Locate and identify every blood parasite.
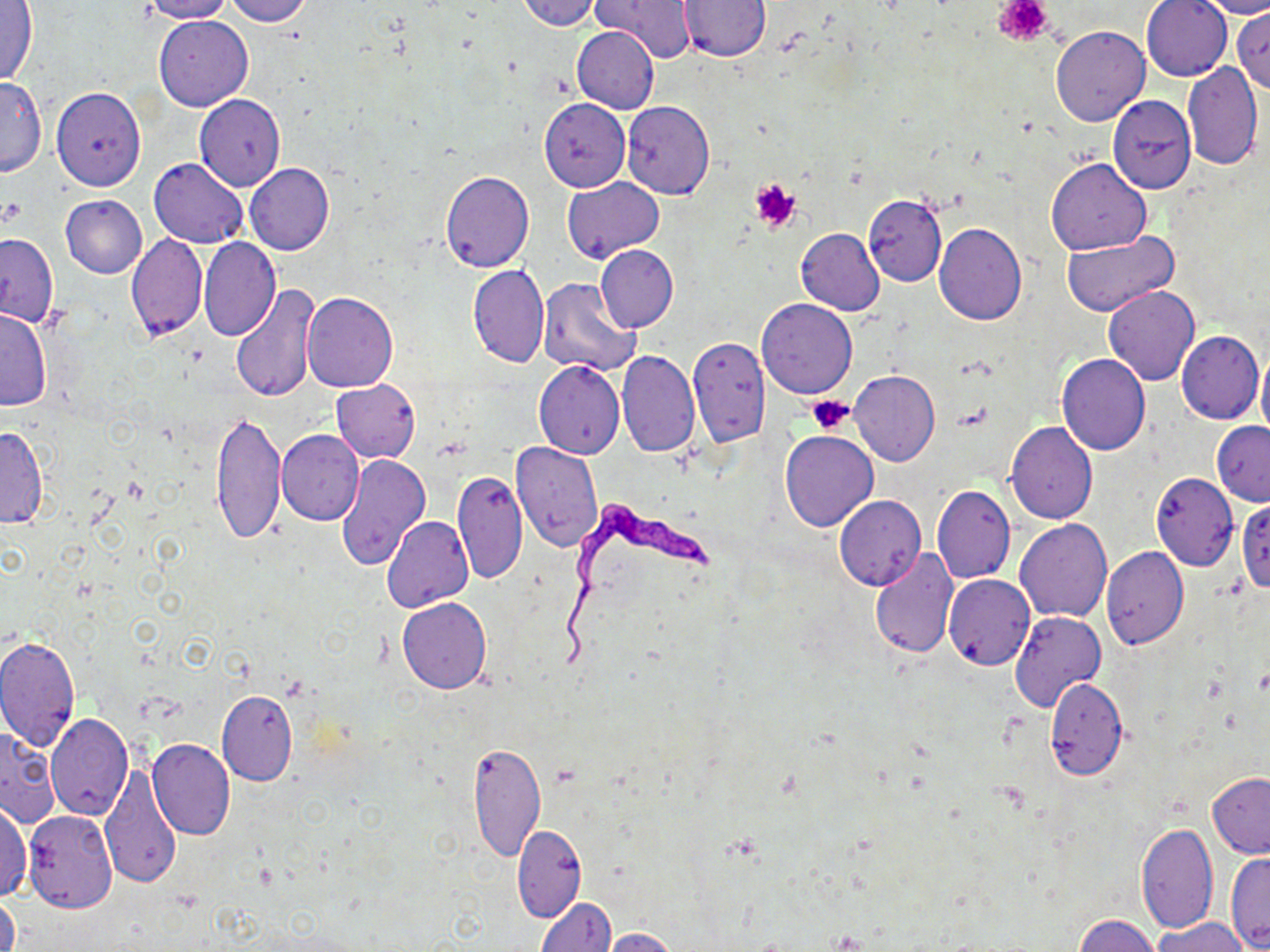
Approximate bounding boxes as named x1/y1/x2/y2 corners in pixels.
Trypanosoma brucei: (x1=558, y1=500, x2=714, y2=676).
No Plasmodium falciparum, Plasmodium ovale, Plasmodium malariae, Plasmodium vivax, or Babesia divergens observed.

slide_level_diagnosis: Trypanosoma brucei
stain: May-Grünwald-Giemsa
platelet_locations: 'approximate bounding boxes as named x1/y1/x2/y2 corners in pixels: (x1=995, y1=0, x2=1053, y2=45), (x1=750, y1=178, x2=801, y2=231), (x1=2, y1=197, x2=24, y2=225), (x1=806, y1=394, x2=855, y2=434)'
image_size: 1270×952 pixels
field_of_view: one of a larger specimen
magnification: 1000x
preparation: thin blood film
modality: optical microscopy
uninfected_red_blood_cell_locations: 'approximate bounding boxes as named x1/y1/x2/y2 corners in pixels: (x1=137, y1=0, x2=235, y2=22), (x1=221, y1=0, x2=312, y2=25), (x1=516, y1=0, x2=600, y2=30), (x1=594, y1=0, x2=696, y2=62), (x1=1141, y1=0, x2=1232, y2=81), (x1=1199, y1=0, x2=1270, y2=19), (x1=1, y1=1, x2=38, y2=87), (x1=679, y1=1, x2=769, y2=61), (x1=1231, y1=10, x2=1270, y2=94), (x1=153, y1=15, x2=252, y2=111), (x1=1049, y1=25, x2=1150, y2=126), (x1=572, y1=27, x2=658, y2=113), (x1=1183, y1=61, x2=1264, y2=171), (x1=0, y1=75, x2=46, y2=176), (x1=51, y1=86, x2=146, y2=190), (x1=194, y1=93, x2=285, y2=191), (x1=1108, y1=96, x2=1196, y2=194), (x1=540, y1=98, x2=630, y2=192), (x1=623, y1=102, x2=716, y2=199), (x1=148, y1=157, x2=247, y2=247), (x1=1046, y1=158, x2=1152, y2=255), (x1=244, y1=163, x2=334, y2=256), (x1=439, y1=171, x2=534, y2=273), (x1=561, y1=177, x2=663, y2=262), (x1=863, y1=193, x2=947, y2=286), (x1=61, y1=195, x2=147, y2=278), (x1=934, y1=223, x2=1027, y2=325), (x1=796, y1=228, x2=884, y2=314), (x1=1062, y1=231, x2=1179, y2=318), (x1=0, y1=232, x2=59, y2=325), (x1=127, y1=235, x2=206, y2=342), (x1=199, y1=237, x2=281, y2=341), (x1=596, y1=243, x2=677, y2=333), (x1=468, y1=264, x2=549, y2=369), (x1=538, y1=278, x2=642, y2=378), (x1=232, y1=284, x2=320, y2=403), (x1=1103, y1=286, x2=1199, y2=385), (x1=302, y1=293, x2=398, y2=392), (x1=757, y1=298, x2=856, y2=398), (x1=0, y1=307, x2=52, y2=412), (x1=1176, y1=331, x2=1263, y2=424), (x1=688, y1=336, x2=770, y2=446), (x1=1257, y1=343, x2=1270, y2=447), (x1=616, y1=350, x2=700, y2=457), (x1=1056, y1=352, x2=1151, y2=455), (x1=534, y1=360, x2=625, y2=459), (x1=850, y1=370, x2=940, y2=466), (x1=331, y1=379, x2=421, y2=462), (x1=210, y1=410, x2=286, y2=545), (x1=1006, y1=421, x2=1097, y2=523), (x1=1212, y1=422, x2=1270, y2=506), (x1=0, y1=425, x2=49, y2=529), (x1=780, y1=429, x2=878, y2=531), (x1=277, y1=430, x2=364, y2=526), (x1=510, y1=441, x2=604, y2=553), (x1=335, y1=453, x2=431, y2=572), (x1=453, y1=468, x2=527, y2=582), (x1=1151, y1=472, x2=1238, y2=570), (x1=932, y1=486, x2=1015, y2=585), (x1=835, y1=495, x2=926, y2=591), (x1=1237, y1=499, x2=1270, y2=593), (x1=382, y1=516, x2=474, y2=613), (x1=1015, y1=520, x2=1112, y2=621), (x1=1101, y1=547, x2=1189, y2=649), (x1=869, y1=548, x2=958, y2=657), (x1=943, y1=575, x2=1034, y2=670), (x1=397, y1=598, x2=491, y2=693), (x1=1011, y1=610, x2=1104, y2=712), (x1=0, y1=635, x2=80, y2=751), (x1=1045, y1=677, x2=1127, y2=780), (x1=217, y1=689, x2=298, y2=785), (x1=45, y1=714, x2=133, y2=820), (x1=0, y1=728, x2=61, y2=829), (x1=146, y1=738, x2=235, y2=841), (x1=469, y1=741, x2=545, y2=863), (x1=100, y1=763, x2=182, y2=892), (x1=1207, y1=772, x2=1270, y2=858), (x1=0, y1=798, x2=31, y2=900), (x1=23, y1=810, x2=118, y2=913), (x1=1137, y1=821, x2=1219, y2=935), (x1=512, y1=824, x2=586, y2=922), (x1=1227, y1=852, x2=1269, y2=951), (x1=1, y1=893, x2=19, y2=952), (x1=536, y1=896, x2=615, y2=952), (x1=1074, y1=914, x2=1159, y2=952), (x1=1151, y1=916, x2=1252, y2=951), (x1=600, y1=927, x2=678, y2=952)'